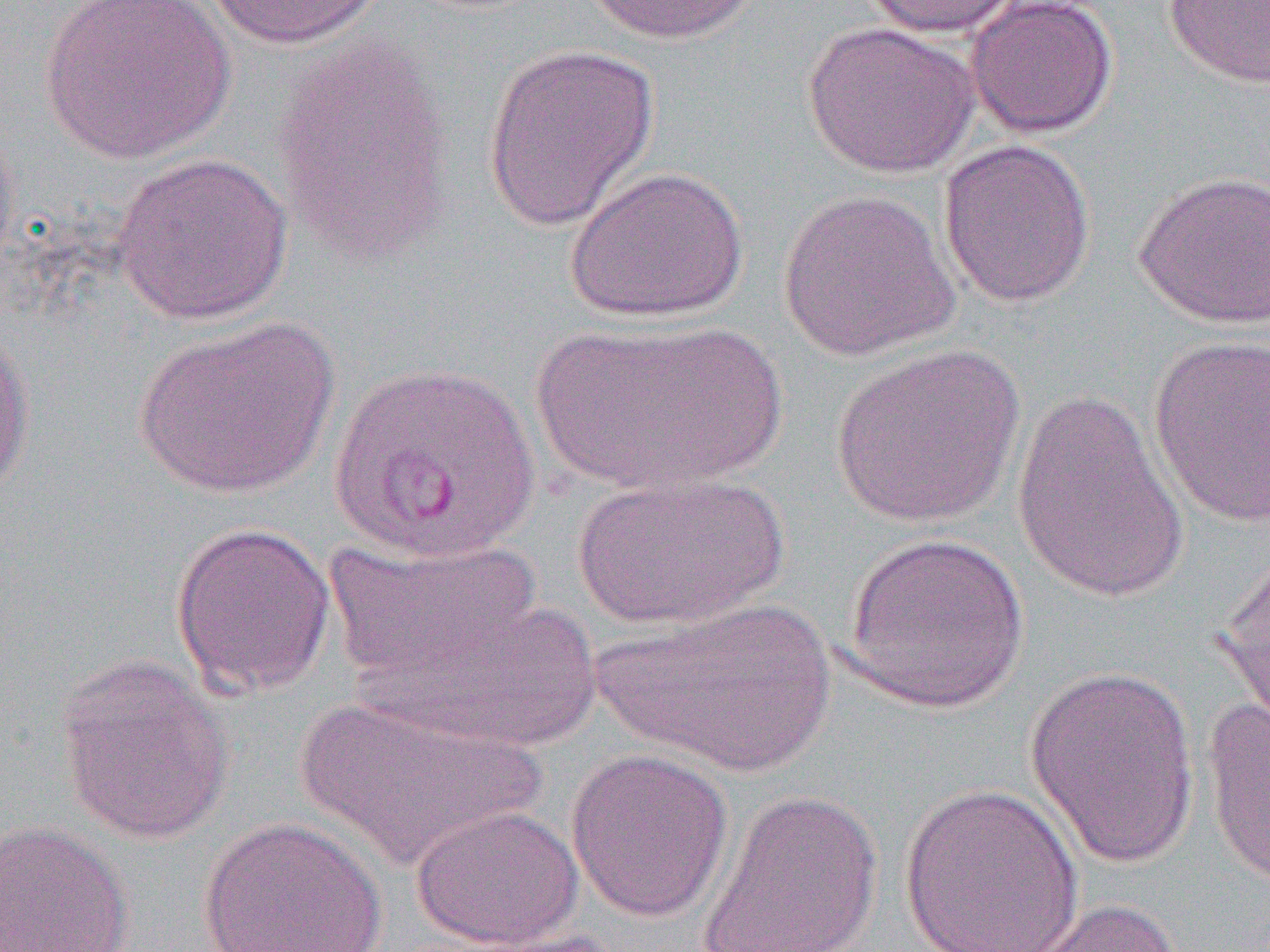

Summary:
  - Coordinate format: approximate bounding boxes as named x1/y1/x2/y2 corners in pixels
  - Uninfected red blood cell locations: (x1=36, y1=0, x2=238, y2=164), (x1=201, y1=0, x2=390, y2=51), (x1=582, y1=0, x2=763, y2=46), (x1=858, y1=0, x2=1025, y2=39), (x1=963, y1=0, x2=1119, y2=139), (x1=1162, y1=0, x2=1270, y2=88), (x1=802, y1=22, x2=980, y2=179), (x1=270, y1=37, x2=457, y2=267), (x1=481, y1=42, x2=660, y2=232), (x1=0, y1=112, x2=20, y2=282), (x1=937, y1=138, x2=1097, y2=308), (x1=110, y1=152, x2=294, y2=326), (x1=566, y1=165, x2=748, y2=323), (x1=1132, y1=169, x2=1270, y2=331), (x1=776, y1=187, x2=960, y2=362), (x1=132, y1=315, x2=341, y2=500), (x1=529, y1=318, x2=788, y2=496), (x1=0, y1=323, x2=36, y2=496), (x1=1147, y1=334, x2=1269, y2=528), (x1=830, y1=344, x2=1025, y2=529), (x1=1011, y1=387, x2=1190, y2=604), (x1=572, y1=471, x2=790, y2=630), (x1=169, y1=520, x2=336, y2=699), (x1=841, y1=531, x2=1031, y2=714), (x1=322, y1=537, x2=548, y2=686), (x1=1213, y1=548, x2=1270, y2=738), (x1=333, y1=580, x2=608, y2=752), (x1=591, y1=595, x2=837, y2=777), (x1=55, y1=653, x2=234, y2=845), (x1=1024, y1=663, x2=1202, y2=870), (x1=291, y1=695, x2=548, y2=871), (x1=1201, y1=696, x2=1270, y2=888), (x1=565, y1=748, x2=734, y2=923), (x1=897, y1=781, x2=1086, y2=952), (x1=696, y1=786, x2=885, y2=952), (x1=410, y1=803, x2=584, y2=951), (x1=198, y1=816, x2=388, y2=952), (x1=0, y1=820, x2=137, y2=952), (x1=1015, y1=897, x2=1185, y2=952)
  - Slide-level diagnosis: Plasmodium vivax
  - Modality: light microscopy
  - Field of view: one of a larger specimen
  - Preparation: thin blood smear
  - Image size: 1270×952 pixels
  - Magnification: 1000x